Give the preparation type.
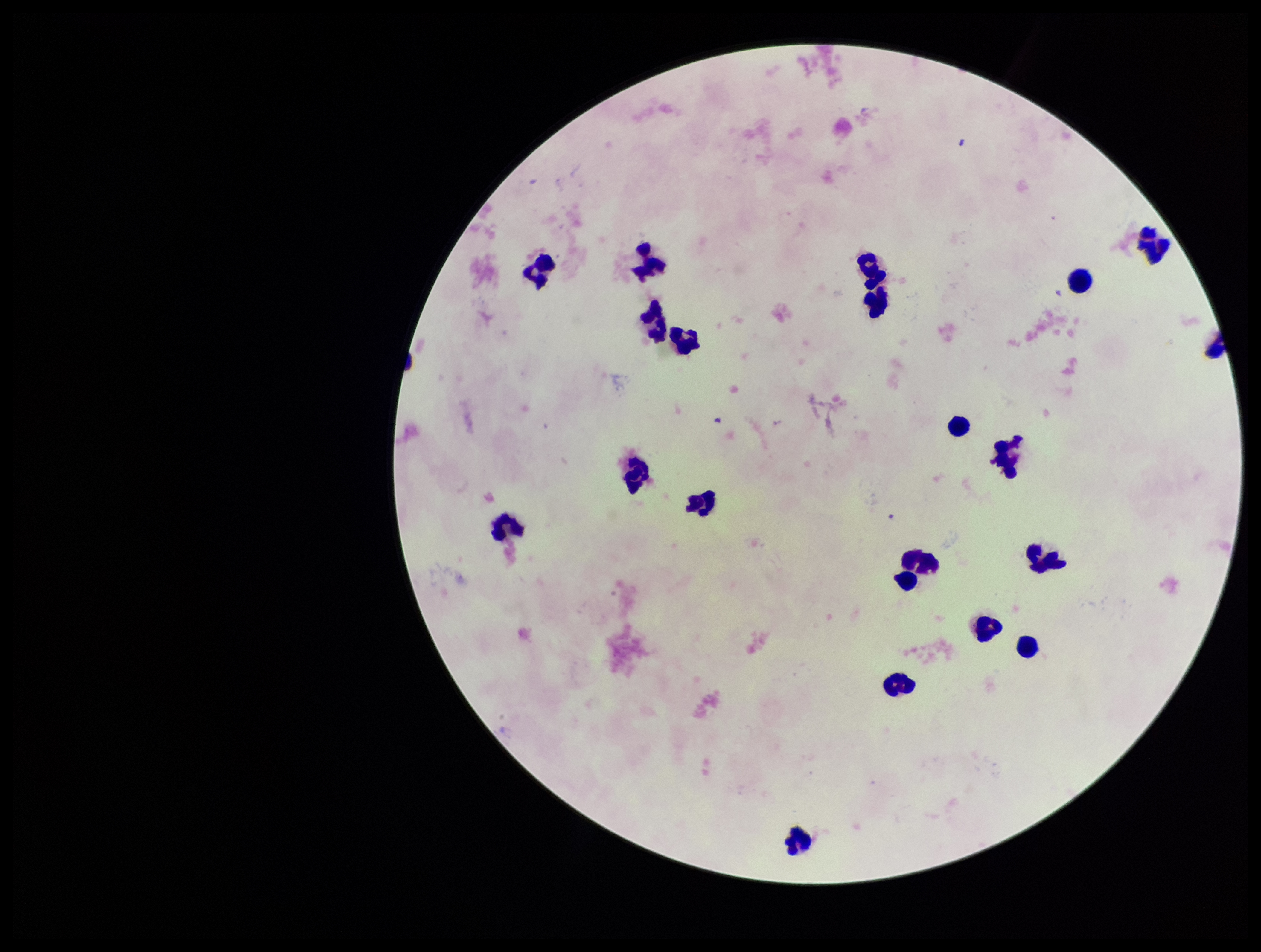
A thick smear.

Summary:
  - Image size: 1261×952 pixels
  - Plasmodium parasites: none detected
  - Stain: Giemsa
  - Leukocyte count: 21
  - Parasite count: 0
  - Field of view: single
  - Patient malaria status: negative
  - Capture: smartphone photograph through the microscope eyepiece